Report the malaria status of this cell.
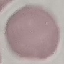

It is uninfected.

Cell patch, automatically extracted from a larger field of view and resized to 64 × 64 pixels. Acquired by smartphone through the microscope eyepiece. Giemsa stain. Thin blood smear.